State which cell type is depicted.
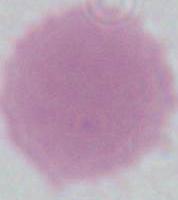

An erythrocyte.

modality: micrograph
magnification: 1000x